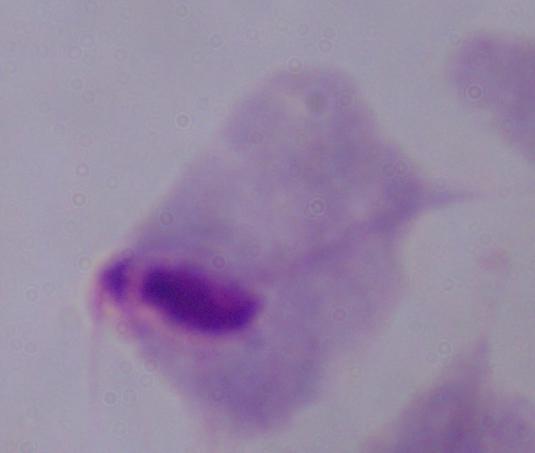
magnification = 1000x
modality = photomicrograph
identification = trichomonad